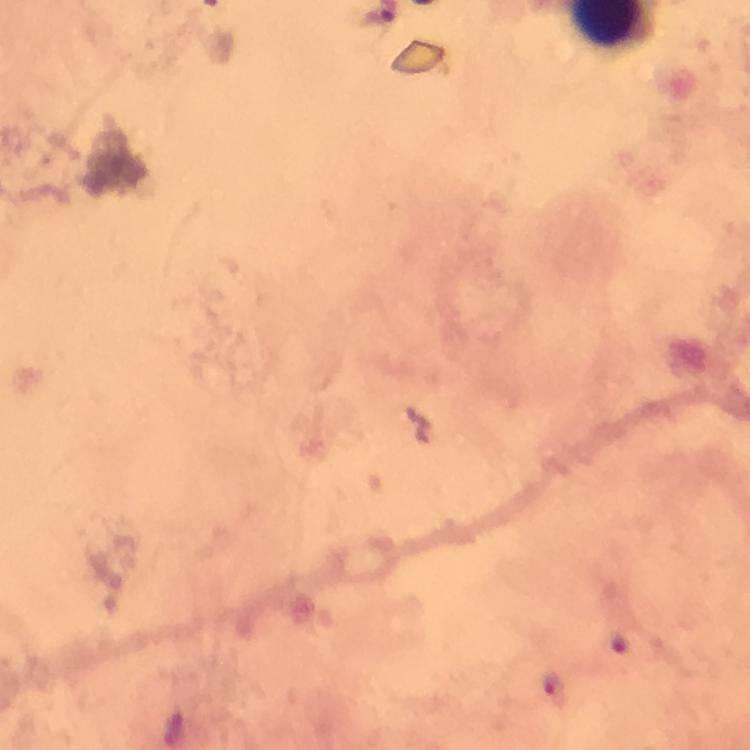
Approximate object centers, in pixels from the top-left corner.
Summary:
  - Plasmodium parasite locations: (x=620, y=645), (x=551, y=686)
  - Stain: Giemsa
  - Magnification: 100x
  - Immersion oil: applied
  - Image size: 750×750 pixels
  - Context: from a malaria diagnostic workup
  - Capture: smartphone mounted on the microscope
  - Cropped from: a single field of view
  - Preparation: thick blood film